Locate and identify every blood parasite.
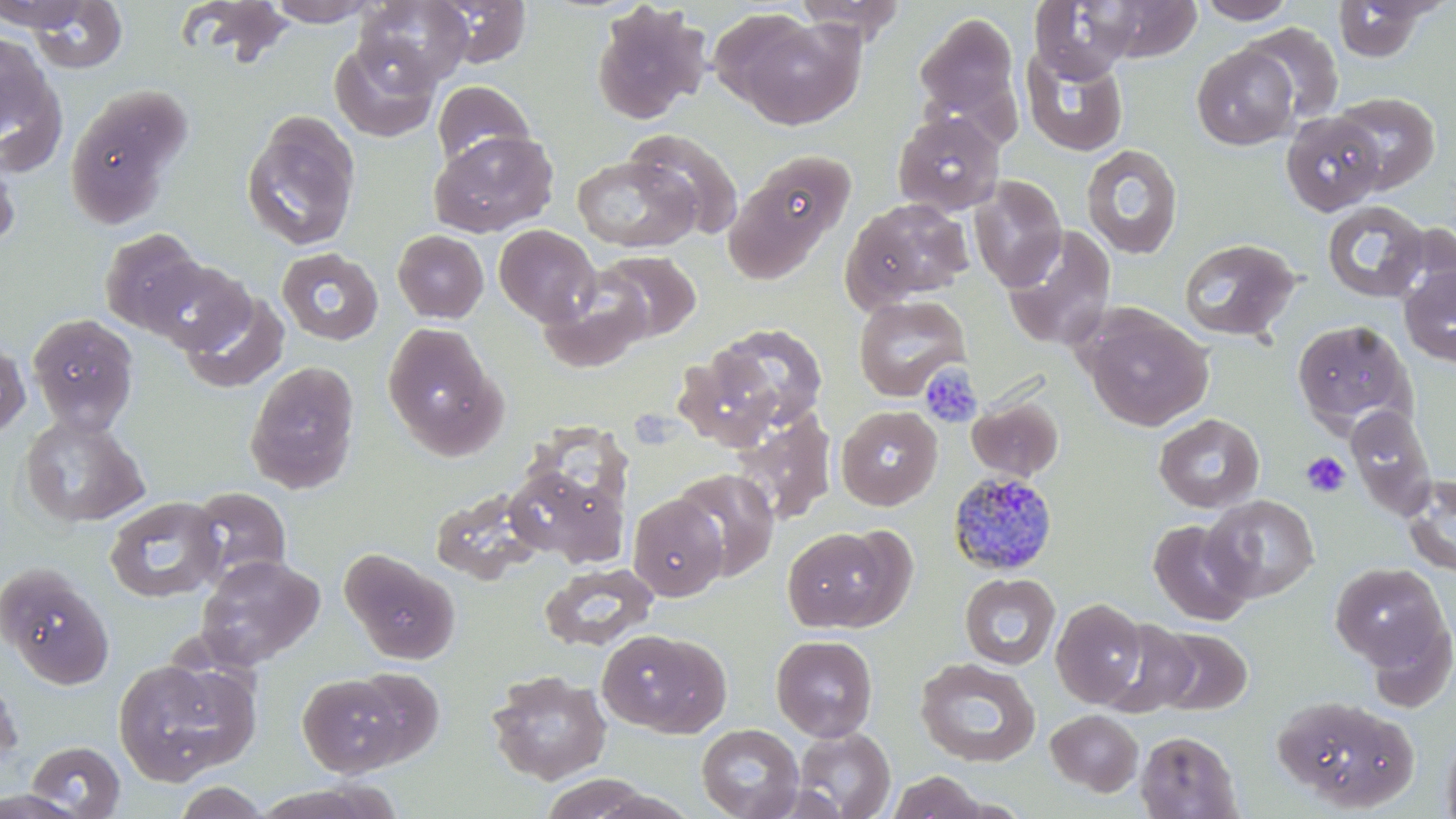
Approximate bounding boxes as (x1, y1, x2, y2) in pixels.
Plasmodium malariae-infected red blood cells: (947, 470, 1058, 576).
No Plasmodium falciparum, Plasmodium ovale, Plasmodium vivax, Babesia divergens, or Trypanosoma brucei observed.

Summary:
  - Uninfected red blood cell locations: (174, 0, 299, 67), (266, 0, 380, 26), (356, 0, 473, 88), (432, 0, 533, 67), (791, 0, 908, 41), (1029, 0, 1139, 82), (0, 1, 95, 31), (25, 1, 129, 74), (1078, 1, 1203, 63), (1194, 1, 1298, 24), (1332, 1, 1437, 62), (590, 3, 710, 125), (718, 11, 865, 130), (913, 11, 1022, 132), (1241, 22, 1344, 125), (0, 32, 53, 138), (329, 38, 441, 142), (1192, 45, 1300, 150), (1020, 47, 1129, 159), (0, 60, 67, 177), (431, 79, 536, 170), (64, 85, 192, 228), (1332, 91, 1441, 194), (240, 111, 361, 252), (892, 111, 1005, 215), (1281, 112, 1387, 215), (626, 128, 746, 238), (429, 130, 557, 237), (1081, 144, 1184, 260), (0, 151, 20, 255), (727, 152, 856, 277), (572, 156, 699, 253), (969, 176, 1067, 292), (842, 198, 975, 307), (1321, 200, 1430, 303), (493, 224, 600, 326), (1002, 226, 1117, 350), (98, 228, 207, 335), (393, 230, 489, 323), (1178, 237, 1301, 342), (276, 248, 384, 346), (596, 250, 701, 342), (139, 258, 253, 354), (1399, 264, 1456, 368), (538, 277, 652, 373), (180, 290, 290, 394), (853, 294, 970, 401), (1079, 305, 1214, 432), (27, 313, 139, 434), (1291, 320, 1417, 435), (382, 322, 506, 458), (706, 323, 829, 435), (0, 337, 30, 439), (244, 360, 361, 494), (966, 394, 1064, 482), (835, 405, 943, 511), (1346, 405, 1437, 520), (729, 408, 837, 526), (1153, 413, 1265, 514), (18, 414, 149, 528), (504, 467, 626, 566), (672, 467, 779, 581), (1400, 473, 1456, 579), (187, 486, 291, 585), (628, 494, 728, 601), (1203, 495, 1319, 602), (104, 496, 226, 603), (1148, 519, 1253, 625), (782, 525, 907, 633), (341, 548, 460, 664), (196, 554, 325, 669), (1329, 561, 1451, 672), (0, 562, 115, 690), (538, 562, 658, 652), (959, 573, 1060, 670), (1051, 597, 1148, 707), (1099, 618, 1200, 718), (597, 627, 731, 737), (1152, 627, 1252, 715), (771, 635, 878, 741), (915, 657, 1042, 767), (112, 658, 256, 786), (350, 667, 445, 765), (486, 671, 612, 785), (0, 673, 22, 776), (297, 673, 406, 777), (1273, 694, 1418, 810), (1045, 709, 1144, 796), (696, 724, 803, 819), (1440, 724, 1456, 819), (793, 727, 896, 818), (1135, 730, 1243, 818), (27, 741, 125, 818), (886, 771, 988, 819), (539, 773, 657, 818), (171, 781, 273, 819), (0, 790, 90, 819)
  - Platelet locations: (919, 363, 983, 428), (1301, 451, 1350, 497)
  - Slide-level diagnosis: Plasmodium malariae
  - Image size: 1456×819 pixels
  - Preparation: thin blood film
  - Magnification: 1000x
  - Modality: optical microscopy
  - Field of view: one of a larger specimen
  - Stain: May-Grünwald-Giemsa